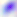
identification: Toxoplasma gondii
magnification: 400x
modality: photomicrograph